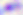
Summary:
  - Identification: Toxoplasma gondii
  - Magnification: 400x
  - Modality: micrograph